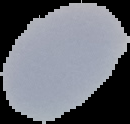
image size = 130×124 pixels
malaria status = uninfected
image type = segmented cell region on a black background
preparation = thin blood film